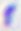
Summary:
  - Modality: micrograph
  - Identification: Toxoplasma gondii
  - Magnification: 400x